Point out every malaria parasite.
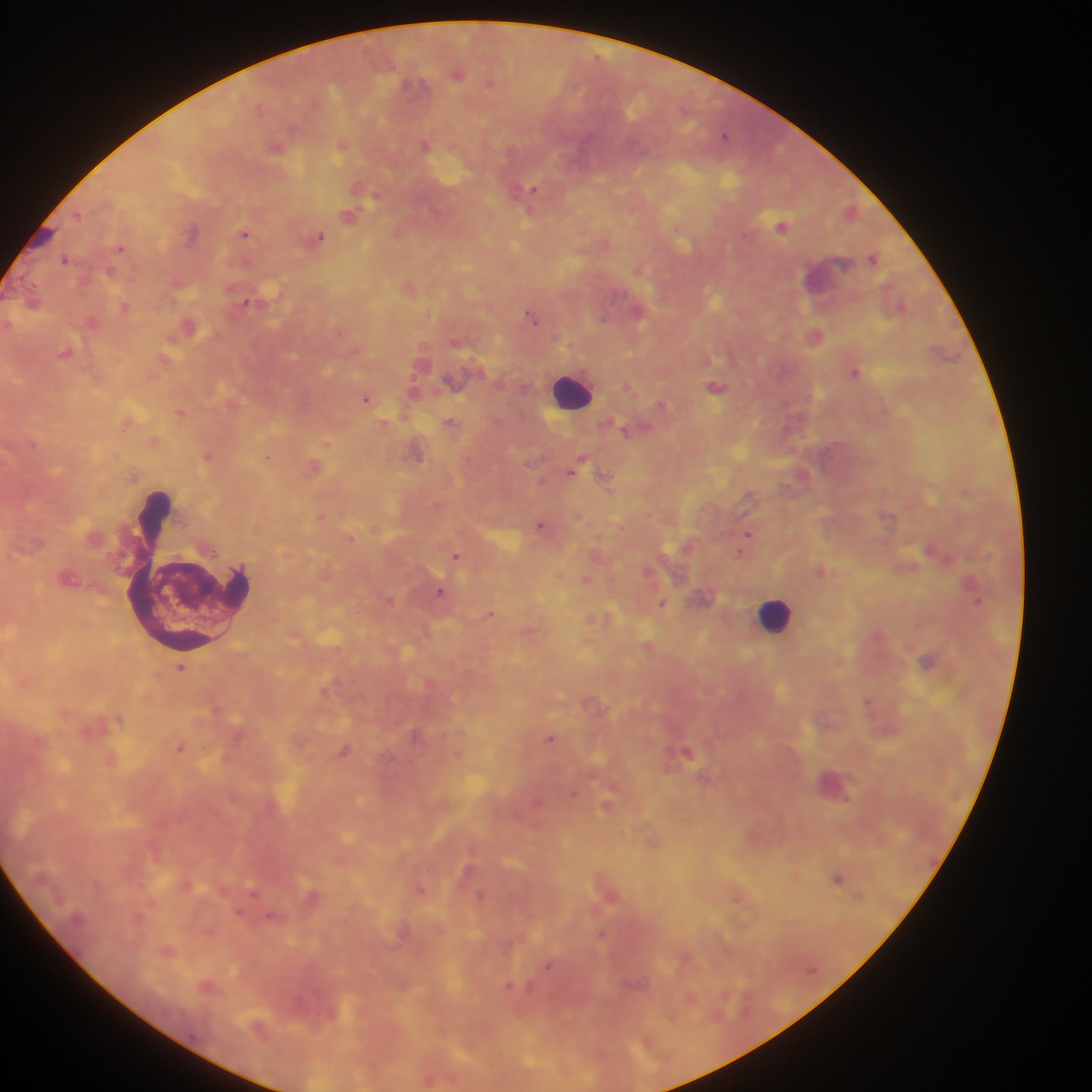
Approximate centers as (x, y) in pixels.
Malaria parasites: (598, 55), (424, 143), (534, 188), (375, 196), (350, 216), (783, 225), (193, 228), (245, 234), (320, 237), (65, 260), (639, 270), (407, 284), (247, 303), (125, 306), (429, 315), (531, 315), (605, 315), (818, 332), (856, 372), (718, 389), (366, 398), (181, 413), (208, 457), (267, 457), (571, 472), (322, 515), (540, 524), (747, 533), (740, 551), (457, 554), (587, 579), (439, 591), (390, 600), (979, 602), (663, 603), (491, 611), (870, 703), (551, 739), (181, 747), (687, 749), (574, 794), (848, 799), (538, 802), (606, 805), (469, 869), (839, 878), (421, 889), (482, 895), (739, 898), (152, 900), (594, 910), (140, 914), (603, 932), (549, 963), (509, 985).

Summary:
  - Leukocyte locations: (578, 394), (184, 573), (773, 613)
  - Preparation: thick blood film
  - Country: Ghana
  - Capture: mobile-phone photograph through a microscope
  - Image size: 1092×1092 pixels
  - Field of view: single